Report the malaria status of this cell.
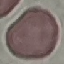

It is uninfected.

capture = smartphone through the microscope eyepiece
stain = Giemsa
image type = automatically extracted cell patch, resized to 64 × 64 pixels
preparation = thin blood film